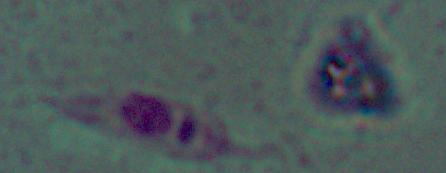

Summary:
  - Identification: Leishmania
  - Magnification: 1000x
  - Modality: photomicrograph